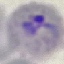

malaria_status: parasitized
capture: smartphone camera at the microscope eyepiece
stain: Giemsa
image_type: cell patch, automatically extracted from a larger field of view and resized to 64 × 64 pixels
preparation: thin smear